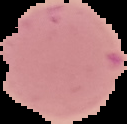

Result: negative for Plasmodium parasites. Image is 127×124 pixels. Segmented cell region on a black background. From a thin blood film.